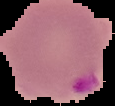
Summary:
  - Image size: 115×106 pixels
  - Malaria status: parasitized
  - Image type: cell region segmented out of the field of view; surrounding area masked to black
  - Preparation: thin blood film